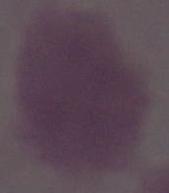
1000x magnification. A red blood cell is shown. Micrograph.